Identify the blood parasite species.
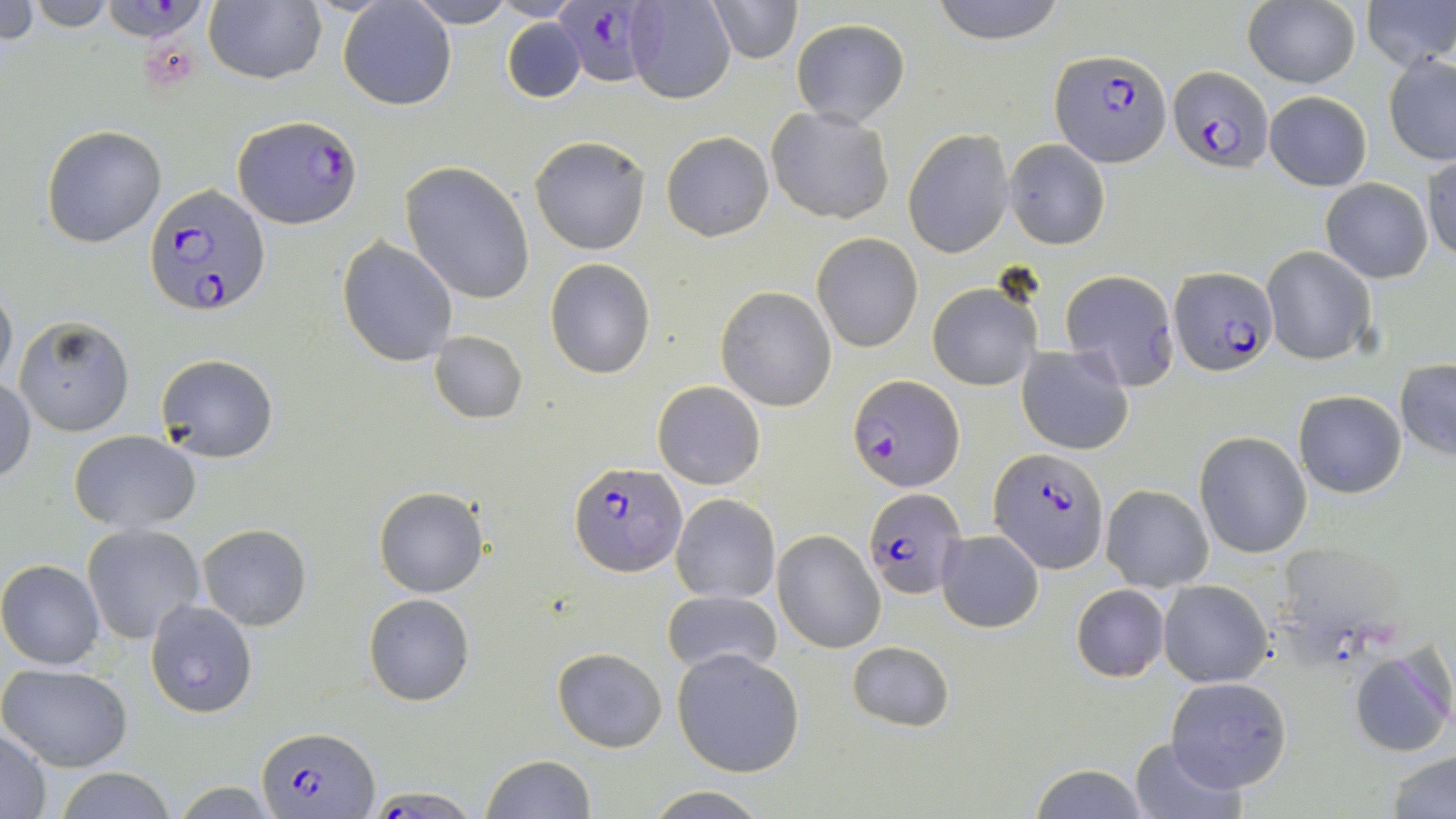

Plasmodium falciparum.

uninfected red blood cell locations = approximate bounding boxes as [x1, y1, x2, y2] in pixels: [0, 0, 38, 49], [24, 0, 118, 30], [337, 0, 456, 111], [406, 0, 518, 28], [706, 0, 803, 64], [930, 0, 1068, 44], [1364, 1, 1454, 72], [204, 2, 326, 85], [626, 2, 737, 105], [1242, 3, 1360, 87], [501, 18, 587, 104], [789, 18, 910, 127], [1383, 54, 1456, 164], [1264, 91, 1372, 191], [765, 106, 896, 225], [41, 125, 167, 248], [903, 127, 1014, 258], [660, 131, 774, 242], [529, 135, 651, 255], [1005, 139, 1111, 250], [1423, 154, 1455, 265], [401, 163, 534, 304], [1320, 178, 1434, 283], [811, 232, 922, 352], [337, 237, 457, 366], [1261, 246, 1377, 366], [545, 258, 655, 380], [1059, 269, 1181, 389], [0, 280, 17, 391], [927, 283, 1042, 391], [715, 286, 837, 412], [14, 316, 134, 436], [429, 330, 527, 424], [1017, 345, 1136, 456], [154, 353, 279, 462], [1395, 359, 1456, 460], [0, 379, 36, 485], [652, 380, 767, 490], [1294, 390, 1407, 498], [68, 430, 202, 533], [1194, 430, 1311, 558], [1101, 484, 1213, 593], [373, 486, 488, 597], [670, 493, 781, 604], [81, 523, 208, 645], [197, 524, 311, 631], [773, 530, 885, 653], [938, 530, 1044, 632], [0, 559, 105, 669], [1159, 580, 1273, 688], [1071, 584, 1169, 682], [661, 588, 783, 675], [364, 593, 475, 706], [148, 598, 256, 717], [847, 640, 954, 732], [1348, 645, 1455, 757], [553, 647, 668, 752], [672, 648, 805, 778], [0, 663, 135, 772], [1167, 676, 1292, 792], [0, 728, 54, 818], [1128, 737, 1245, 818], [1386, 748, 1455, 819], [481, 754, 598, 818], [1029, 763, 1150, 819], [55, 767, 177, 819], [640, 788, 773, 818]
field of view = one of a larger specimen
Plasmodium falciparum-infected red blood cell locations = approximate bounding boxes as [x1, y1, x2, y2] in pixels: [102, 0, 205, 44], [551, 0, 659, 88], [1050, 50, 1170, 167], [1169, 64, 1271, 171], [233, 113, 360, 229], [146, 183, 268, 317], [1168, 267, 1278, 378], [846, 373, 963, 493], [990, 447, 1108, 573], [570, 462, 685, 577], [864, 487, 968, 599], [257, 724, 378, 815], [360, 786, 483, 818]
preparation = thin blood film
image size = 1456×819 pixels
magnification = 1000x
stain = May-Grünwald-Giemsa
modality = light microscopy